Classify this cell by malaria status.
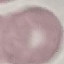
It is uninfected.

Summary:
  - Preparation: thin smear
  - Capture: smartphone through the microscope eyepiece
  - Stain: Giemsa
  - Image type: cell patch, automatically extracted from a larger field of view and resized to 64 × 64 pixels